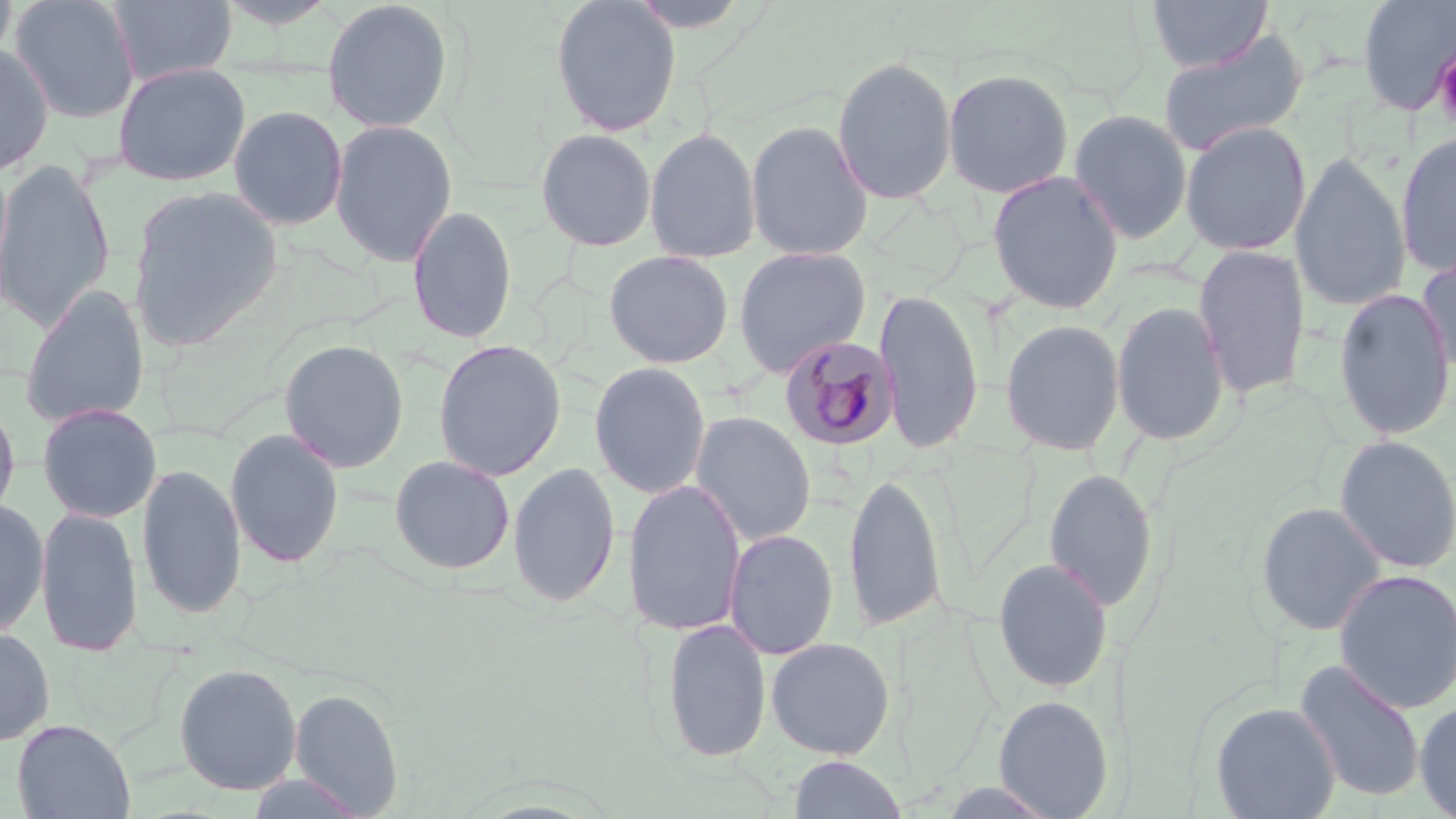

Summary:
  - Coordinate format: approximate bounding boxes as named x1/y1/x2/y2 corners in pixels
  - Platelet locations: (x1=1434, y1=48, x2=1456, y2=129)
  - Uninfected red blood cell locations: (x1=0, y1=0, x2=17, y2=73), (x1=9, y1=0, x2=140, y2=123), (x1=107, y1=0, x2=237, y2=87), (x1=321, y1=0, x2=454, y2=133), (x1=550, y1=0, x2=682, y2=137), (x1=1146, y1=0, x2=1272, y2=73), (x1=1356, y1=0, x2=1456, y2=116), (x1=209, y1=2, x2=344, y2=29), (x1=1156, y1=29, x2=1309, y2=156), (x1=0, y1=44, x2=54, y2=177), (x1=831, y1=55, x2=958, y2=205), (x1=112, y1=61, x2=251, y2=186), (x1=942, y1=67, x2=1074, y2=199), (x1=228, y1=104, x2=349, y2=231), (x1=1068, y1=109, x2=1193, y2=244), (x1=330, y1=119, x2=458, y2=267), (x1=746, y1=119, x2=873, y2=261), (x1=1180, y1=121, x2=1311, y2=256), (x1=645, y1=126, x2=761, y2=263), (x1=535, y1=128, x2=657, y2=251), (x1=1396, y1=131, x2=1456, y2=279), (x1=1290, y1=151, x2=1411, y2=313), (x1=0, y1=157, x2=16, y2=317), (x1=0, y1=158, x2=116, y2=332), (x1=986, y1=170, x2=1125, y2=314), (x1=127, y1=185, x2=284, y2=351), (x1=406, y1=204, x2=517, y2=344), (x1=1192, y1=243, x2=1311, y2=401), (x1=732, y1=245, x2=872, y2=377), (x1=603, y1=250, x2=734, y2=369), (x1=1416, y1=251, x2=1456, y2=384), (x1=19, y1=285, x2=149, y2=429), (x1=874, y1=287, x2=984, y2=456), (x1=1333, y1=287, x2=1455, y2=441), (x1=1110, y1=300, x2=1230, y2=446), (x1=999, y1=318, x2=1124, y2=456), (x1=279, y1=338, x2=409, y2=473), (x1=432, y1=339, x2=566, y2=482), (x1=589, y1=361, x2=711, y2=499), (x1=0, y1=394, x2=20, y2=532), (x1=37, y1=403, x2=161, y2=523), (x1=690, y1=411, x2=816, y2=547), (x1=225, y1=427, x2=345, y2=569), (x1=1334, y1=435, x2=1456, y2=574), (x1=389, y1=454, x2=515, y2=575), (x1=507, y1=461, x2=620, y2=608), (x1=136, y1=462, x2=247, y2=620), (x1=1043, y1=467, x2=1159, y2=611), (x1=843, y1=470, x2=946, y2=634), (x1=622, y1=479, x2=747, y2=637), (x1=0, y1=500, x2=50, y2=639), (x1=1256, y1=501, x2=1387, y2=636), (x1=35, y1=506, x2=143, y2=657), (x1=723, y1=529, x2=839, y2=660), (x1=993, y1=558, x2=1113, y2=693), (x1=1332, y1=568, x2=1456, y2=714), (x1=661, y1=617, x2=771, y2=763), (x1=0, y1=626, x2=55, y2=746), (x1=765, y1=637, x2=896, y2=760), (x1=1293, y1=659, x2=1427, y2=803), (x1=173, y1=662, x2=303, y2=796), (x1=289, y1=687, x2=404, y2=815), (x1=992, y1=694, x2=1115, y2=818), (x1=1414, y1=699, x2=1456, y2=818), (x1=1210, y1=701, x2=1341, y2=819), (x1=11, y1=718, x2=136, y2=819), (x1=787, y1=755, x2=908, y2=818)
  - Plasmodium malariae-infected red blood cell locations: (x1=779, y1=336, x2=901, y2=451)
  - Slide-level diagnosis: Plasmodium malariae
  - Preparation: thin blood smear
  - Image size: 1456×819 pixels
  - Magnification: 1000x
  - Modality: light microscopy
  - Stain: May-Grünwald-Giemsa
  - Field of view: single